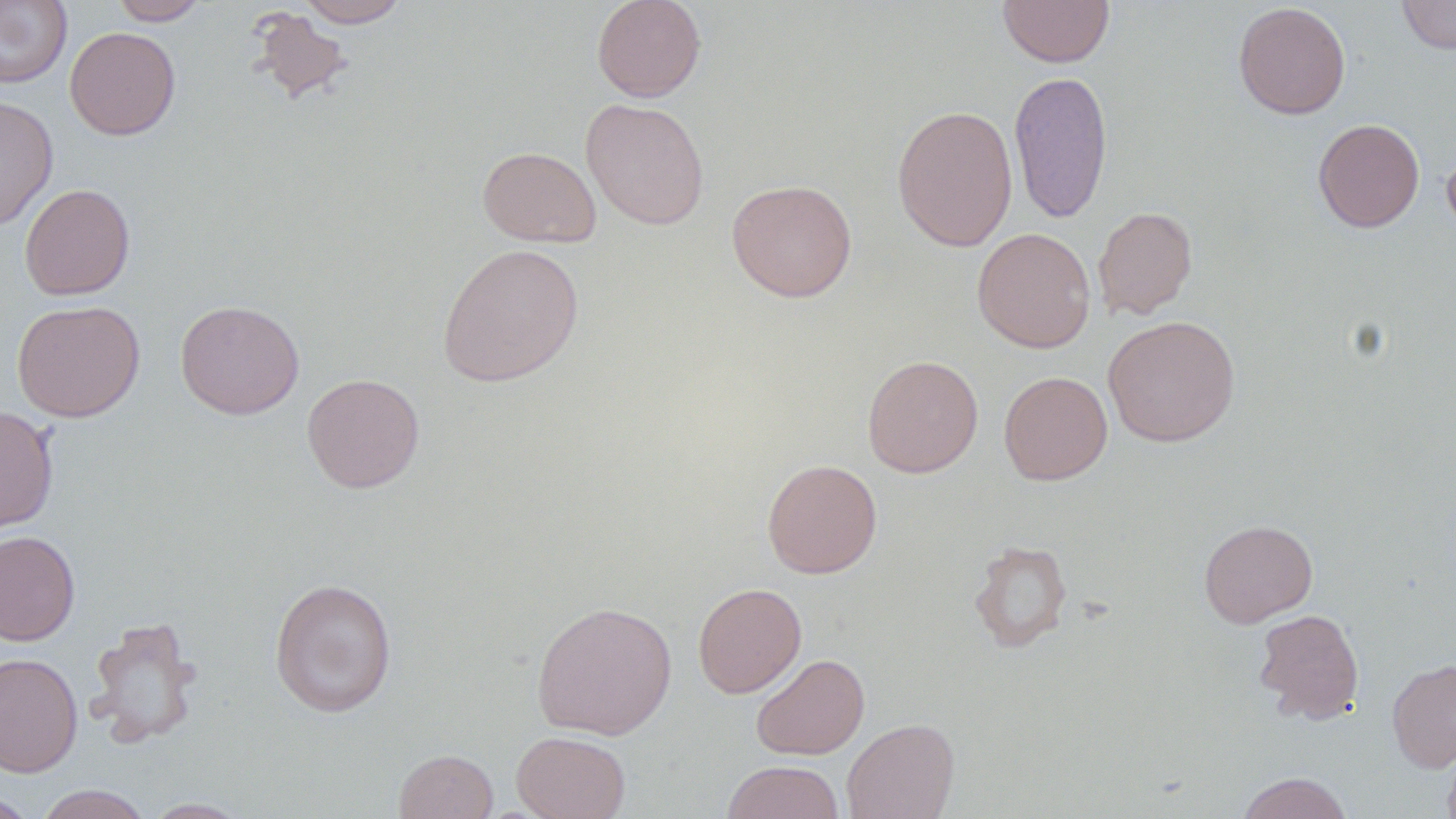
Approximate bounding boxes as (x1,y1)-(x2,y2) corner pairs in pixels. Uninfected red blood cell locations: (0,0)-(72,88), (111,0)-(209,25), (296,0)-(410,27), (591,0)-(707,102), (997,0)-(1114,67), (1397,0)-(1456,54), (1232,2)-(1351,119), (248,8)-(355,105), (64,27)-(181,140), (1008,69)-(1113,223), (0,95)-(59,230), (581,98)-(710,230), (891,104)-(1018,252), (1313,118)-(1425,233), (1442,143)-(1456,241), (477,146)-(602,247), (726,179)-(857,302), (20,183)-(135,300), (1093,205)-(1199,320), (972,226)-(1095,353), (437,243)-(584,388), (11,299)-(145,422), (175,299)-(304,419), (1102,315)-(1240,447), (862,355)-(983,478), (998,370)-(1113,485), (302,373)-(424,494), (0,405)-(59,533), (762,459)-(882,578), (1199,519)-(1318,628), (0,530)-(80,645), (968,539)-(1072,653), (269,577)-(397,718), (692,582)-(807,698), (531,600)-(678,740), (1253,608)-(1365,724), (85,615)-(203,748), (0,652)-(83,778), (751,653)-(870,760), (1387,658)-(1456,772), (842,717)-(960,819), (511,731)-(630,819), (1442,736)-(1456,819), (393,748)-(498,819), (722,760)-(845,819), (1236,771)-(1354,819), (34,784)-(152,819), (0,792)-(39,819), (140,797)-(254,818). Slide-level diagnosis: negative for blood parasites. Light microscopy. Thin blood smear. Single field of view. Captured at 1000x magnification. Image is 1456×819 pixels. May-Grünwald-Giemsa-stained preparation.